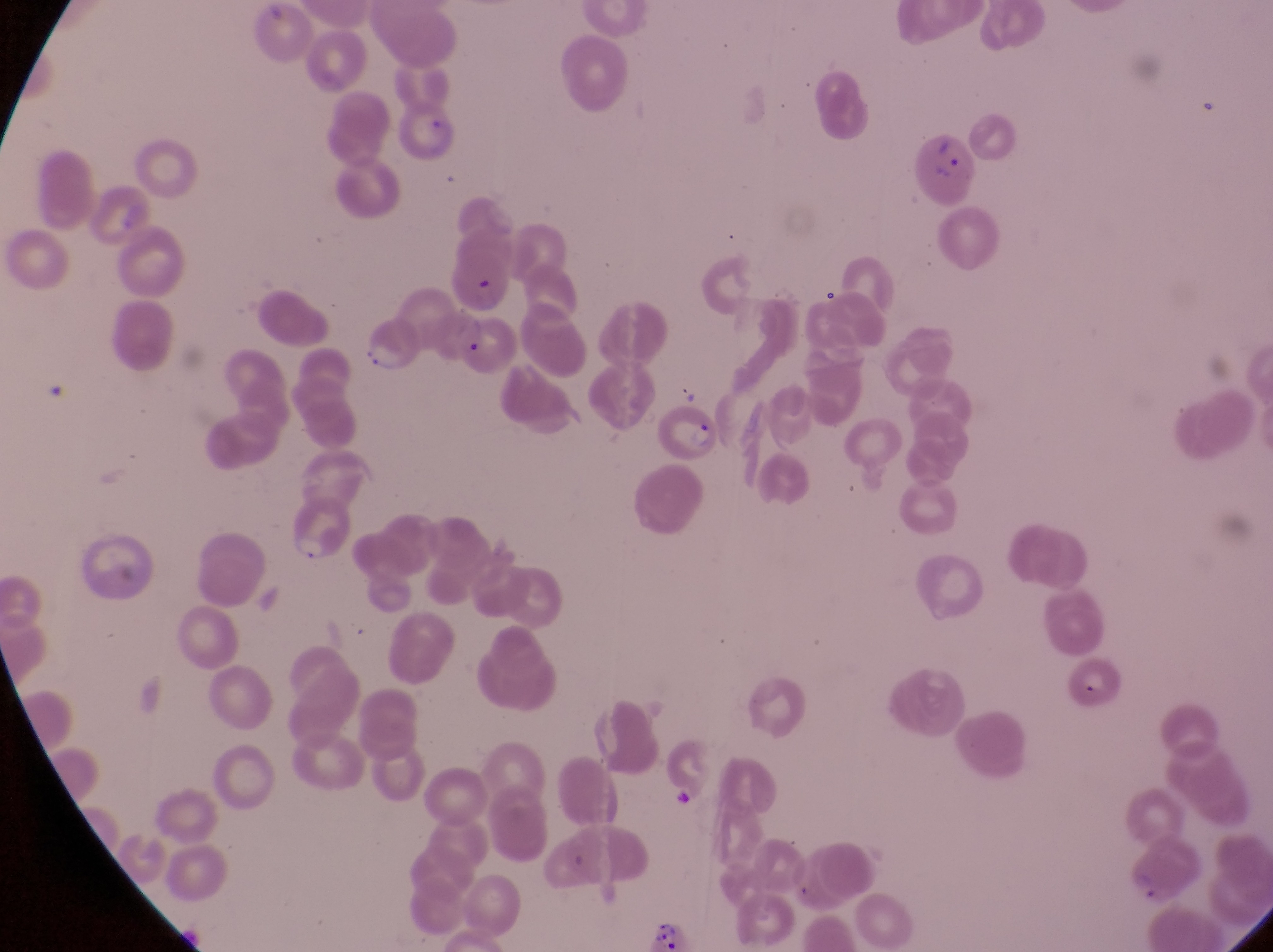

country = Uganda
trophozoite locations = approximate bounding boxes as left top right bottom in pixels: 289 524 324 564
parasitised red blood cell locations = approximate bounding boxes as left top right bottom in pixels: 444 244 511 316; 356 305 426 375; 460 324 517 379; 659 404 717 461
capture = smartphone photograph through the eyepiece of an Olympus CX-23 microscope
artifact (platelet-like body, stain precipitate, or debris) locations = approximate bounding boxes as left top right bottom in pixels: 936 142 969 192; 667 791 692 813; 646 913 693 952
preparation = thin blood film
field of view = single
magnification = 1000x
image size = 1273×952 pixels